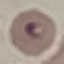
malaria status = parasitized
preparation = thin blood smear
capture = smartphone camera at the microscope eyepiece
stain = Giemsa
image type = cell patch, automatically extracted from a larger field of view and resized to 64 × 64 pixels